Classify this cell by malaria status.
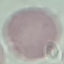
It is uninfected.

Thin smear of blood. Cell patch, automatically extracted from a larger field of view and resized to 64 × 64 pixels. Acquired by smartphone through the microscope eyepiece. Giemsa-stained preparation.